Report the malaria status of this cell.
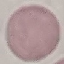
Uninfected.

image type = cell patch, automatically extracted from a larger field of view and resized to 64 × 64 pixels
stain = Giemsa
preparation = thin smear
capture = smartphone camera at the microscope eyepiece